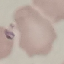
malaria status = parasitized
preparation = thin blood smear
image type = automatically extracted cell patch, resized to 64 × 64 pixels
capture = smartphone through the microscope eyepiece
stain = Giemsa